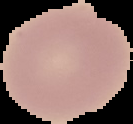

Summary:
  - Image type: segmented cell region on a black background
  - Malaria status: uninfected
  - Image size: 133×124 pixels
  - Preparation: thin blood film